Find the cells and give the type of each one.
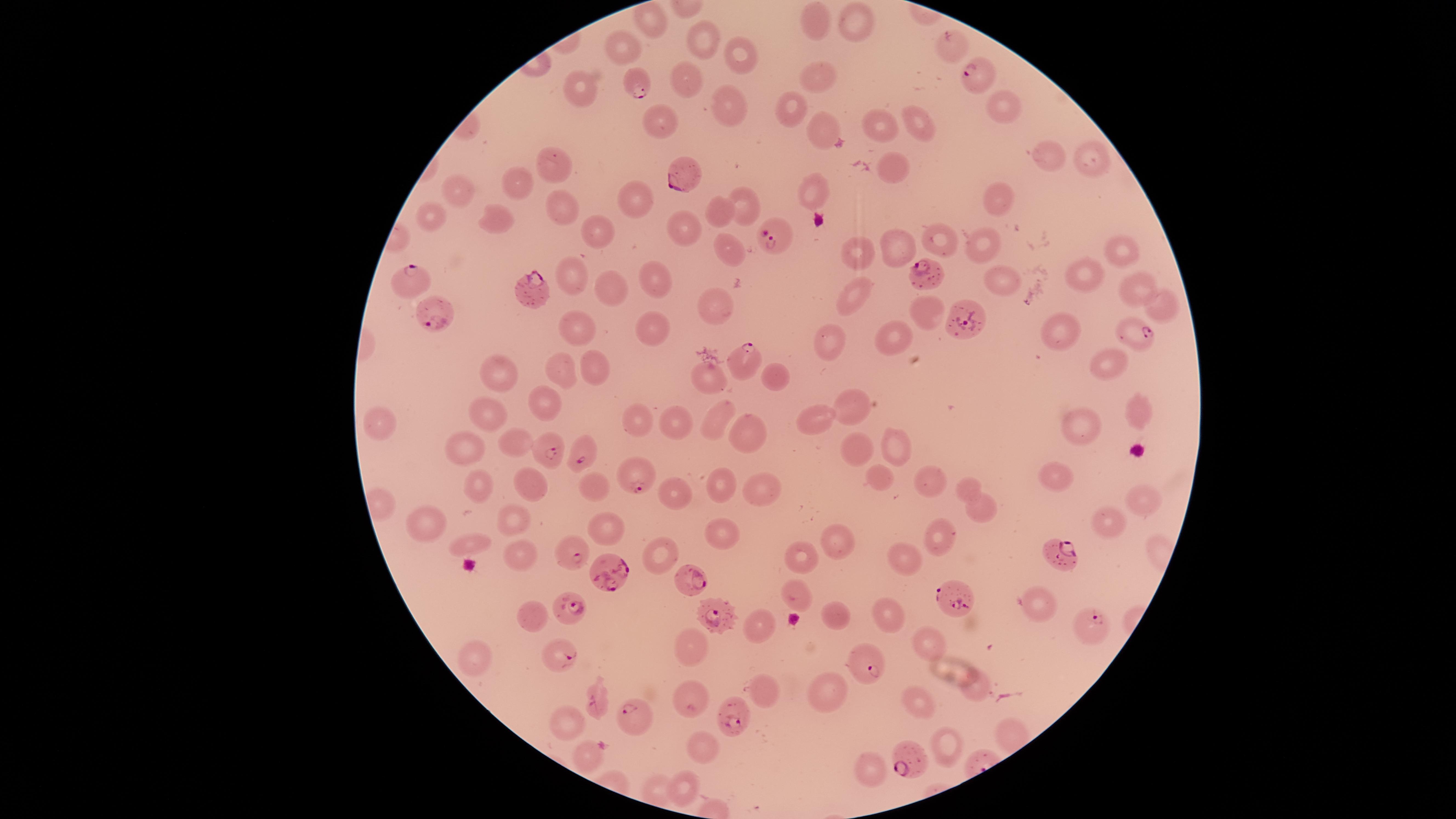
Approximate marker points as [x, y] in pixels.
Parasitized red blood cells: [980, 74], [637, 82], [680, 174], [775, 236], [926, 270], [411, 285], [532, 287], [438, 316], [961, 317], [1133, 334], [738, 362], [547, 451], [580, 455], [633, 475], [573, 553], [1059, 553], [610, 573], [691, 579], [961, 598], [573, 604], [720, 616], [1093, 629], [563, 654], [865, 658], [598, 703], [630, 717], [736, 718], [911, 753].
Uninfected red blood cells: [651, 18], [817, 18], [851, 23], [702, 39], [953, 43], [624, 48], [741, 56], [818, 72], [682, 77], [583, 85], [999, 99], [722, 106], [790, 107], [660, 124], [918, 125], [881, 127], [822, 129], [1090, 155], [1050, 157], [553, 164], [894, 168], [518, 177], [459, 188], [813, 188], [627, 198], [1000, 198], [556, 203], [744, 206], [432, 212], [720, 212], [492, 223], [686, 223], [592, 232], [940, 238], [897, 243], [980, 243], [1116, 250], [733, 253], [861, 253], [1084, 277], [1001, 278], [572, 279], [656, 279], [1137, 282], [608, 291], [856, 295], [720, 301], [1161, 305], [927, 308], [654, 321], [579, 325], [893, 332], [1060, 333], [834, 341], [1112, 363], [559, 365], [592, 366], [711, 373], [501, 375], [776, 376], [850, 400], [541, 404], [1134, 405], [487, 410], [382, 416], [640, 417], [817, 417], [713, 418], [677, 422], [1079, 427], [751, 432], [518, 442], [897, 444], [858, 446], [472, 451], [877, 473], [1055, 478], [721, 481], [927, 481], [530, 483], [479, 484], [764, 486], [964, 486], [590, 487], [674, 490], [1145, 501], [979, 513], [512, 515], [1109, 520], [432, 523], [606, 527], [721, 530], [937, 532], [837, 539], [468, 542], [516, 550], [801, 554], [657, 558], [905, 558], [797, 590], [1036, 597], [889, 606], [835, 610], [528, 614], [761, 623], [694, 641], [927, 642], [471, 652], [974, 683], [826, 689], [763, 694], [690, 701], [917, 703], [566, 717], [945, 745], [703, 749], [587, 757], [871, 764], [680, 784].
No white blood cells identified.

Image is 1456×819 pixels. Circular visible region. Smartphone photograph through the microscope eyepiece. Giemsa stain. Thin smear of blood. Species: Plasmodium falciparum. One field of view of the specimen.